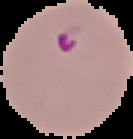

Summary:
  - Preparation: thin blood film
  - Image type: cell region segmented out of the field of view; surrounding area masked to black
  - Result: Plasmodium parasites detected
  - Image size: 133×139 pixels